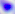
Toxoplasma gondii is shown. Micrograph. Captured at 400x magnification.